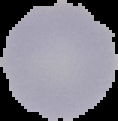
{
  "image_size": "118×121 pixels",
  "result": "no Plasmodium parasites seen",
  "preparation": "thin blood film",
  "image_type": "segmented cell region on a black background"
}